Name the parasite shown.
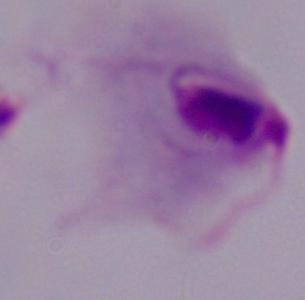
This is a trichomonad.

Captured at 1000x magnification. Photomicrograph.